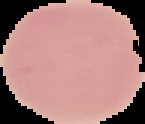 The area outside the segmented cell region is set to black. Image is 145×124 pixels. Result: negative for Plasmodium parasites. From a thin blood smear.